Give the extent of all uninfected red blood cells.
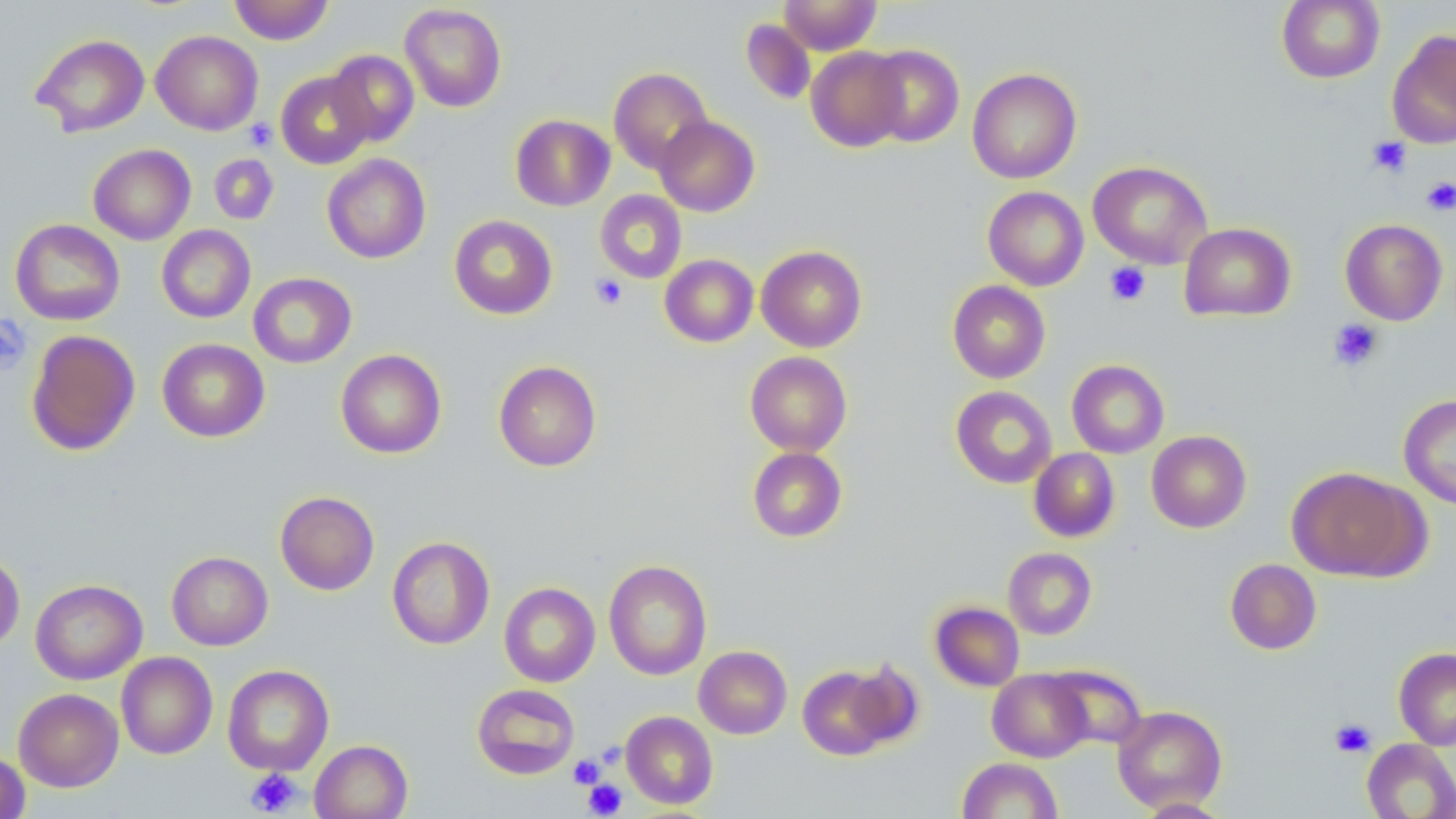
Approximate bounding boxes as (x1, y1, x2, y2) in pixels.
Uninfected red blood cells: (229, 0, 335, 45), (779, 0, 881, 54), (1276, 0, 1385, 84), (399, 3, 507, 112), (740, 19, 816, 105), (1386, 28, 1456, 149), (151, 30, 263, 135), (30, 33, 150, 137), (863, 44, 965, 147), (806, 47, 909, 152), (326, 49, 420, 146), (608, 67, 713, 175), (967, 67, 1081, 184), (276, 70, 375, 169), (510, 114, 615, 211), (654, 116, 760, 216), (88, 144, 196, 245), (209, 154, 278, 225), (322, 154, 431, 264), (1088, 160, 1213, 269), (983, 186, 1089, 291), (595, 190, 687, 284), (448, 214, 558, 319), (10, 219, 125, 326), (1340, 219, 1448, 325), (1179, 222, 1296, 321), (156, 225, 256, 324), (756, 245, 867, 352), (660, 254, 758, 347), (248, 272, 357, 368), (948, 280, 1050, 383), (25, 329, 141, 456), (157, 338, 270, 442), (336, 349, 447, 458), (745, 351, 852, 456), (1067, 359, 1169, 458), (493, 360, 602, 472), (950, 386, 1057, 488), (1399, 394, 1456, 510), (1146, 430, 1251, 532), (747, 447, 847, 542), (1029, 448, 1120, 543), (1287, 466, 1426, 582), (275, 491, 379, 595), (387, 536, 495, 650), (1003, 547, 1097, 640), (0, 551, 25, 652), (166, 551, 273, 651), (1225, 558, 1321, 654), (603, 560, 712, 680), (30, 579, 147, 684), (499, 582, 600, 687), (929, 601, 1025, 691), (694, 645, 792, 739), (1393, 648, 1456, 750), (116, 652, 217, 760), (843, 660, 924, 748), (222, 664, 334, 775), (797, 664, 898, 760), (1045, 664, 1146, 749), (987, 669, 1092, 762), (472, 683, 580, 779), (13, 688, 124, 792), (1112, 705, 1227, 812), (621, 711, 718, 809), (1362, 738, 1456, 819), (309, 739, 412, 819), (0, 751, 30, 818), (957, 757, 1063, 818), (1135, 797, 1232, 818).

slide-level diagnosis = negative for blood parasites
stain = May-Grünwald-Giemsa
preparation = thin blood smear
image size = 1456×819 pixels
magnification = 1000x
modality = light microscopy
field of view = single
platelet locations = approximate bounding boxes as (x1, y1, x2, y2) in pixels: (244, 119, 277, 151), (1366, 136, 1412, 177), (1421, 177, 1456, 215), (1104, 262, 1151, 306), (590, 273, 628, 311), (0, 314, 31, 375), (1328, 319, 1384, 372), (1329, 718, 1376, 758), (569, 754, 606, 789), (245, 768, 302, 816), (583, 779, 627, 817)